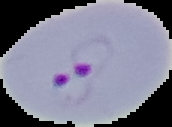

Segmented cell region on a black background. From a thin blood film. Result: malaria parasites identified. Image is 172×127 pixels.